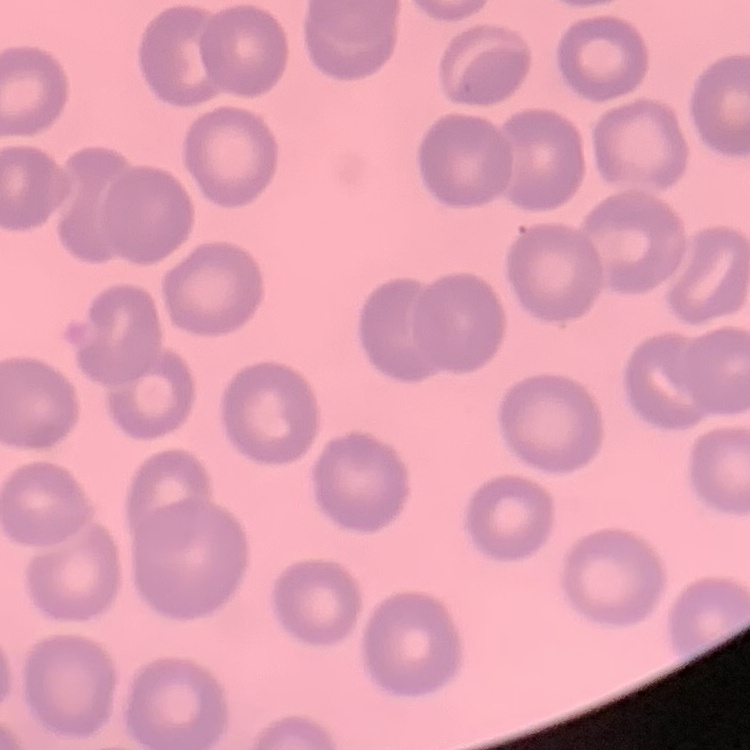
Summary:
  - Erythrocyte morphology: no rouleaux formation
  - Image type: square crop of a larger photomicrograph
  - Stain: Field's or Giemsa
  - Preparation: thin blood smear